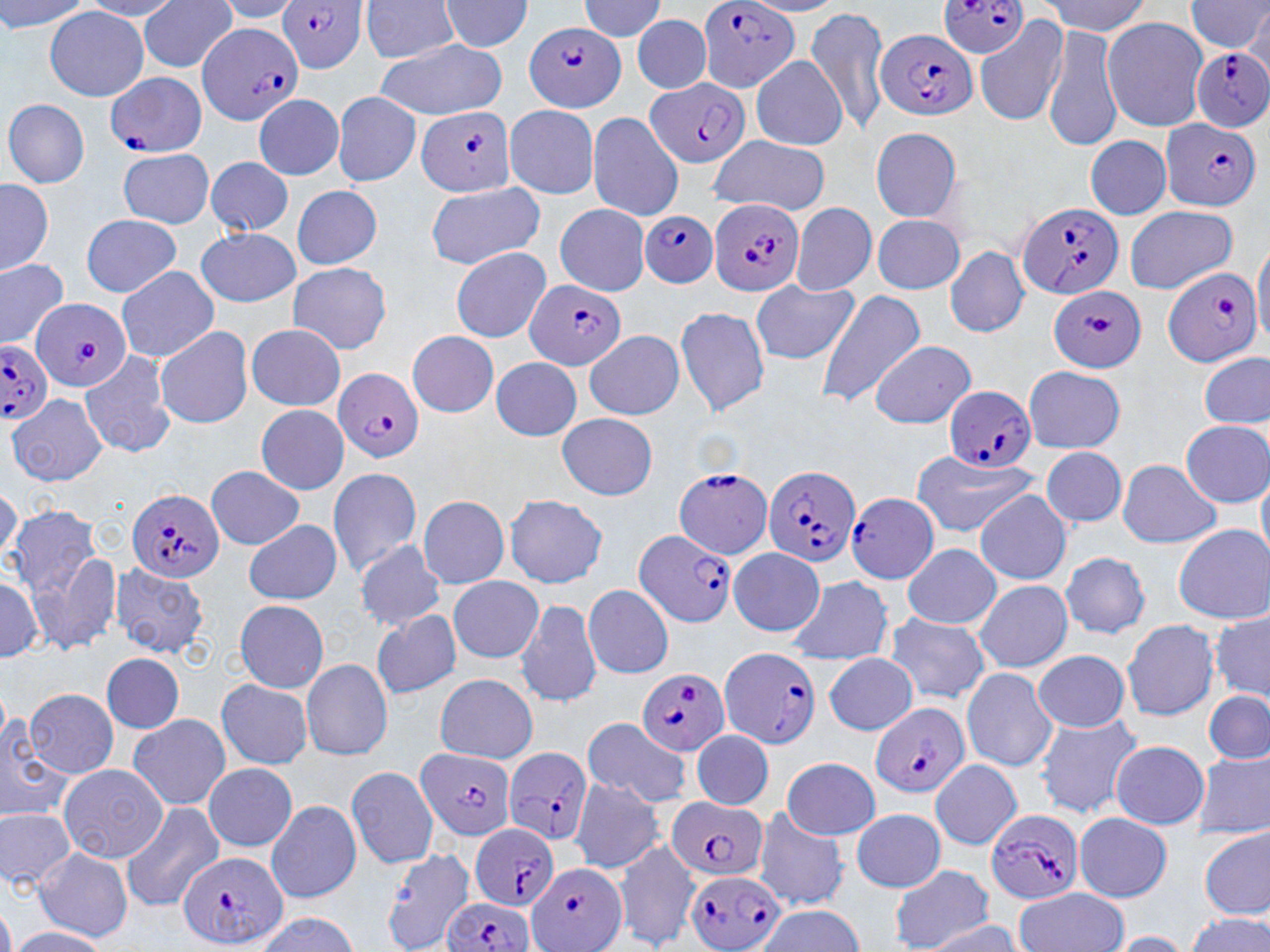
Summary:
  - Coordinate format: approximate bounding boxes as [x1, y1, x2, y2] in pixels
  - Plasmodium falciparum-infected red blood cell locations: [701, 0, 798, 91], [934, 0, 1033, 59], [278, 1, 367, 73], [521, 21, 629, 110], [195, 22, 299, 118], [879, 29, 979, 124], [1195, 44, 1270, 134], [104, 67, 206, 160], [646, 78, 750, 168], [413, 102, 515, 194], [1158, 117, 1262, 209], [707, 193, 805, 298], [1018, 199, 1124, 296], [643, 211, 716, 286], [1165, 265, 1263, 369], [525, 281, 624, 369], [1049, 287, 1147, 368], [26, 294, 129, 395], [0, 339, 53, 428], [332, 366, 428, 462], [942, 383, 1039, 470], [764, 461, 859, 565], [673, 464, 776, 562], [128, 489, 225, 584], [848, 492, 938, 588], [630, 527, 737, 625], [716, 644, 821, 741], [638, 667, 728, 758], [870, 701, 970, 799], [411, 744, 519, 838], [505, 745, 595, 840], [666, 797, 772, 883], [986, 810, 1084, 906], [472, 822, 560, 912], [179, 847, 285, 947], [524, 856, 630, 948], [682, 869, 787, 949], [437, 898, 537, 952]
  - Uninfected red blood cell locations: [576, 0, 666, 43], [365, 1, 457, 64], [42, 6, 147, 100], [805, 8, 891, 135], [1102, 15, 1210, 132], [1043, 26, 1126, 151], [980, 28, 1065, 127], [376, 40, 507, 119], [748, 55, 846, 153], [250, 92, 342, 181], [334, 93, 421, 185], [8, 98, 87, 182], [507, 105, 595, 197], [592, 114, 681, 219], [869, 124, 968, 221], [1085, 133, 1170, 220], [708, 139, 826, 214], [121, 151, 214, 229], [209, 157, 291, 234], [0, 178, 52, 275], [429, 182, 545, 268], [295, 188, 379, 266], [1124, 201, 1241, 293], [790, 202, 880, 299], [557, 204, 647, 298], [80, 213, 180, 295], [870, 213, 963, 293], [198, 228, 299, 305], [946, 247, 1031, 339], [453, 248, 551, 341], [1, 258, 67, 347], [286, 264, 389, 354], [117, 268, 218, 362], [752, 278, 857, 367], [816, 288, 922, 408], [670, 300, 768, 417], [249, 325, 342, 411], [157, 326, 251, 428], [410, 330, 498, 418], [586, 334, 683, 421], [868, 343, 978, 429], [1197, 349, 1270, 433], [492, 360, 581, 441], [80, 361, 174, 458], [1020, 364, 1123, 456], [9, 391, 102, 488], [256, 404, 352, 495], [557, 413, 656, 501], [1178, 416, 1270, 509], [1042, 445, 1127, 528], [1113, 459, 1222, 553], [907, 462, 1044, 537], [208, 466, 304, 550], [330, 469, 420, 575], [974, 488, 1075, 590], [501, 489, 605, 586], [419, 495, 508, 591], [8, 505, 117, 653], [244, 520, 343, 605], [1170, 523, 1270, 624], [355, 538, 444, 632], [901, 543, 1003, 629], [1060, 546, 1150, 642], [729, 547, 824, 639], [115, 562, 209, 661], [450, 575, 545, 663], [788, 575, 894, 672], [969, 578, 1077, 678], [586, 580, 671, 684], [514, 600, 600, 710], [234, 602, 329, 692], [371, 609, 463, 702], [886, 610, 994, 705], [1119, 612, 1214, 723], [1205, 615, 1269, 699], [1032, 648, 1133, 731], [822, 652, 915, 734], [104, 655, 184, 734], [299, 656, 391, 761], [961, 669, 1059, 772], [433, 675, 537, 768], [216, 679, 315, 769], [26, 685, 116, 778], [1199, 691, 1269, 764], [0, 709, 76, 823], [127, 715, 229, 809], [1030, 719, 1146, 821], [581, 725, 694, 810], [691, 729, 772, 811], [1112, 740, 1215, 830], [1195, 753, 1270, 839], [784, 756, 880, 838], [349, 760, 438, 871], [930, 760, 1021, 850], [58, 762, 165, 865], [200, 764, 297, 854], [571, 779, 664, 876], [264, 798, 365, 906], [119, 803, 215, 905], [850, 803, 944, 895], [753, 805, 850, 910], [1078, 810, 1171, 902], [0, 812, 72, 897], [1203, 824, 1268, 912], [613, 836, 695, 952], [380, 846, 471, 950], [36, 848, 136, 942], [889, 866, 993, 952], [1014, 886, 1128, 952]
  - Slide-level diagnosis: Plasmodium falciparum
  - Magnification: 1000x
  - Stain: May-Grünwald-Giemsa
  - Modality: optical microscopy
  - Field of view: single
  - Image size: 1270×952 pixels
  - Preparation: thin blood film